State the blood parasite species.
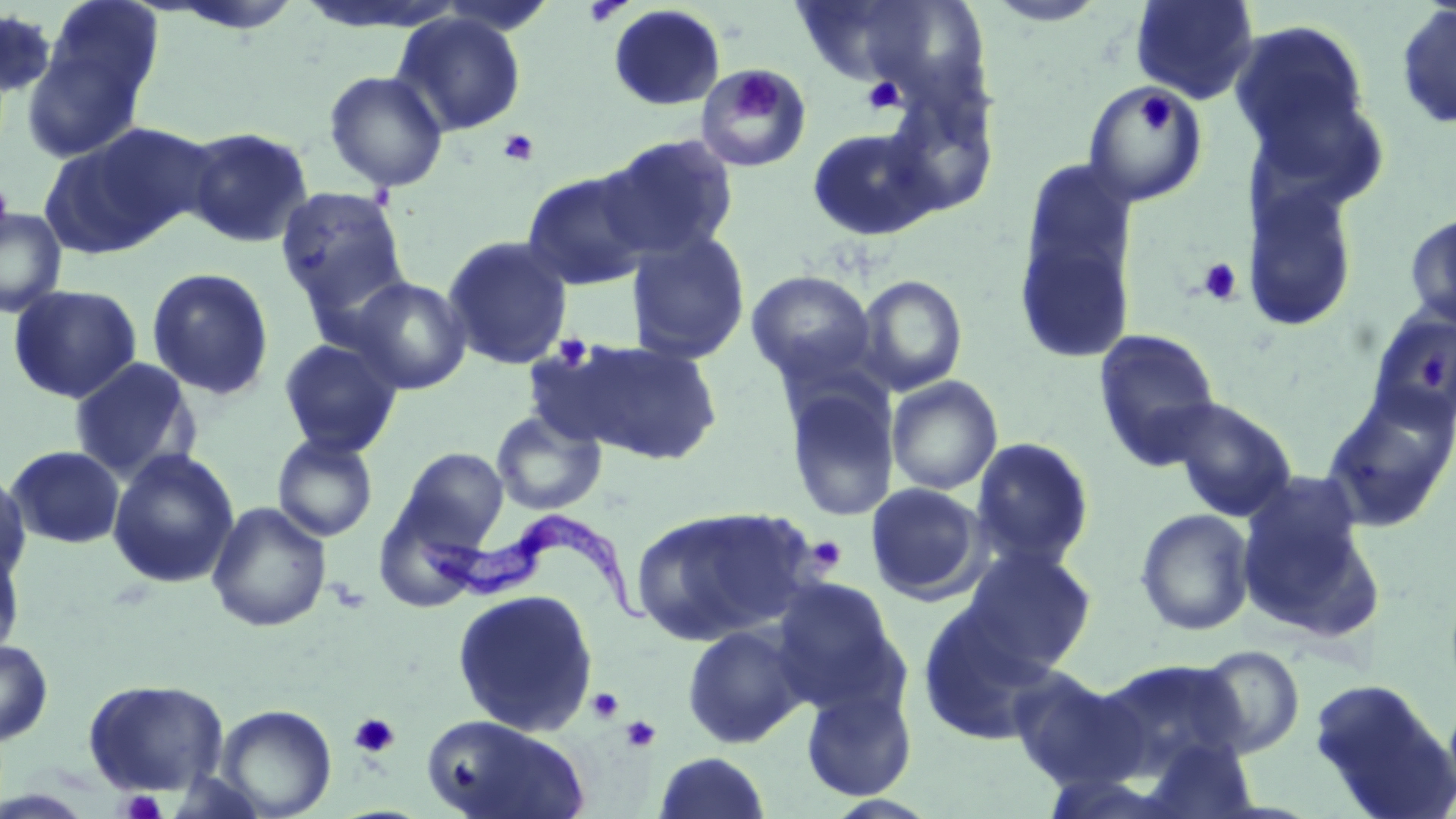

Trypanosoma brucei.

platelet locations = approximate bounding boxes as named x1/y1/x2/y2 corners in pixels: (x1=583, y1=1, x2=632, y2=27), (x1=732, y1=72, x2=778, y2=118), (x1=862, y1=76, x2=905, y2=114), (x1=1138, y1=93, x2=1175, y2=135), (x1=498, y1=129, x2=540, y2=168), (x1=1197, y1=258, x2=1243, y2=305), (x1=551, y1=333, x2=594, y2=369), (x1=1420, y1=354, x2=1446, y2=393), (x1=807, y1=535, x2=847, y2=573), (x1=587, y1=686, x2=625, y2=724), (x1=349, y1=712, x2=400, y2=758), (x1=621, y1=715, x2=660, y2=752), (x1=119, y1=789, x2=168, y2=819)
Trypanosoma brucei locations = approximate bounding boxes as named x1/y1/x2/y2 corners in pixels: (x1=410, y1=510, x2=660, y2=625)
uninfected red blood cell locations = approximate bounding boxes as named x1/y1/x2/y2 corners in pixels: (x1=44, y1=0, x2=165, y2=109), (x1=435, y1=0, x2=558, y2=35), (x1=790, y1=0, x2=945, y2=88), (x1=1130, y1=0, x2=1259, y2=105), (x1=158, y1=1, x2=306, y2=34), (x1=981, y1=1, x2=1110, y2=27), (x1=1395, y1=3, x2=1456, y2=130), (x1=608, y1=4, x2=726, y2=111), (x1=2, y1=8, x2=57, y2=100), (x1=391, y1=12, x2=527, y2=137), (x1=1230, y1=20, x2=1372, y2=160), (x1=19, y1=39, x2=149, y2=162), (x1=696, y1=63, x2=811, y2=171), (x1=323, y1=70, x2=449, y2=192), (x1=1240, y1=78, x2=1393, y2=220), (x1=1082, y1=82, x2=1209, y2=206), (x1=42, y1=122, x2=210, y2=255), (x1=183, y1=127, x2=313, y2=248), (x1=806, y1=127, x2=941, y2=241), (x1=598, y1=133, x2=739, y2=263), (x1=521, y1=169, x2=657, y2=291), (x1=1013, y1=179, x2=1139, y2=366), (x1=1242, y1=182, x2=1361, y2=332), (x1=275, y1=186, x2=411, y2=317), (x1=0, y1=207, x2=67, y2=318), (x1=1404, y1=211, x2=1456, y2=330), (x1=625, y1=230, x2=751, y2=365), (x1=442, y1=235, x2=574, y2=370), (x1=147, y1=267, x2=275, y2=400), (x1=746, y1=270, x2=877, y2=385), (x1=856, y1=274, x2=968, y2=395), (x1=349, y1=276, x2=472, y2=395), (x1=7, y1=284, x2=143, y2=404), (x1=1366, y1=307, x2=1456, y2=426), (x1=1093, y1=329, x2=1223, y2=470), (x1=278, y1=338, x2=402, y2=457), (x1=558, y1=338, x2=724, y2=465), (x1=68, y1=357, x2=201, y2=482), (x1=886, y1=376, x2=1003, y2=495), (x1=782, y1=380, x2=900, y2=522), (x1=1320, y1=383, x2=1456, y2=534), (x1=1166, y1=398, x2=1298, y2=521), (x1=491, y1=409, x2=607, y2=515), (x1=272, y1=433, x2=378, y2=541), (x1=970, y1=437, x2=1095, y2=570), (x1=6, y1=445, x2=125, y2=550), (x1=395, y1=446, x2=510, y2=551), (x1=107, y1=448, x2=240, y2=589), (x1=0, y1=467, x2=32, y2=585), (x1=1235, y1=476, x2=1383, y2=640), (x1=866, y1=482, x2=986, y2=603), (x1=206, y1=501, x2=333, y2=632), (x1=631, y1=505, x2=816, y2=646), (x1=1135, y1=508, x2=1255, y2=636), (x1=0, y1=539, x2=26, y2=662), (x1=958, y1=546, x2=1097, y2=673), (x1=770, y1=578, x2=903, y2=710), (x1=451, y1=588, x2=599, y2=736), (x1=916, y1=607, x2=1064, y2=745), (x1=681, y1=623, x2=809, y2=749), (x1=0, y1=640, x2=53, y2=746), (x1=1195, y1=645, x2=1305, y2=758), (x1=1094, y1=658, x2=1252, y2=780), (x1=1007, y1=668, x2=1141, y2=792), (x1=1307, y1=677, x2=1454, y2=818), (x1=82, y1=678, x2=230, y2=796), (x1=799, y1=683, x2=917, y2=802), (x1=216, y1=704, x2=337, y2=818), (x1=420, y1=715, x2=590, y2=819), (x1=1140, y1=735, x2=1260, y2=818), (x1=653, y1=751, x2=772, y2=818)
image size = 1456×819 pixels
modality = optical microscopy
preparation = thin blood film
field of view = one of a larger specimen
stain = May-Grünwald-Giemsa
magnification = 1000x